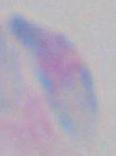
Summary:
  - Magnification: 1000x
  - Identification: Toxoplasma gondii
  - Modality: photomicrograph